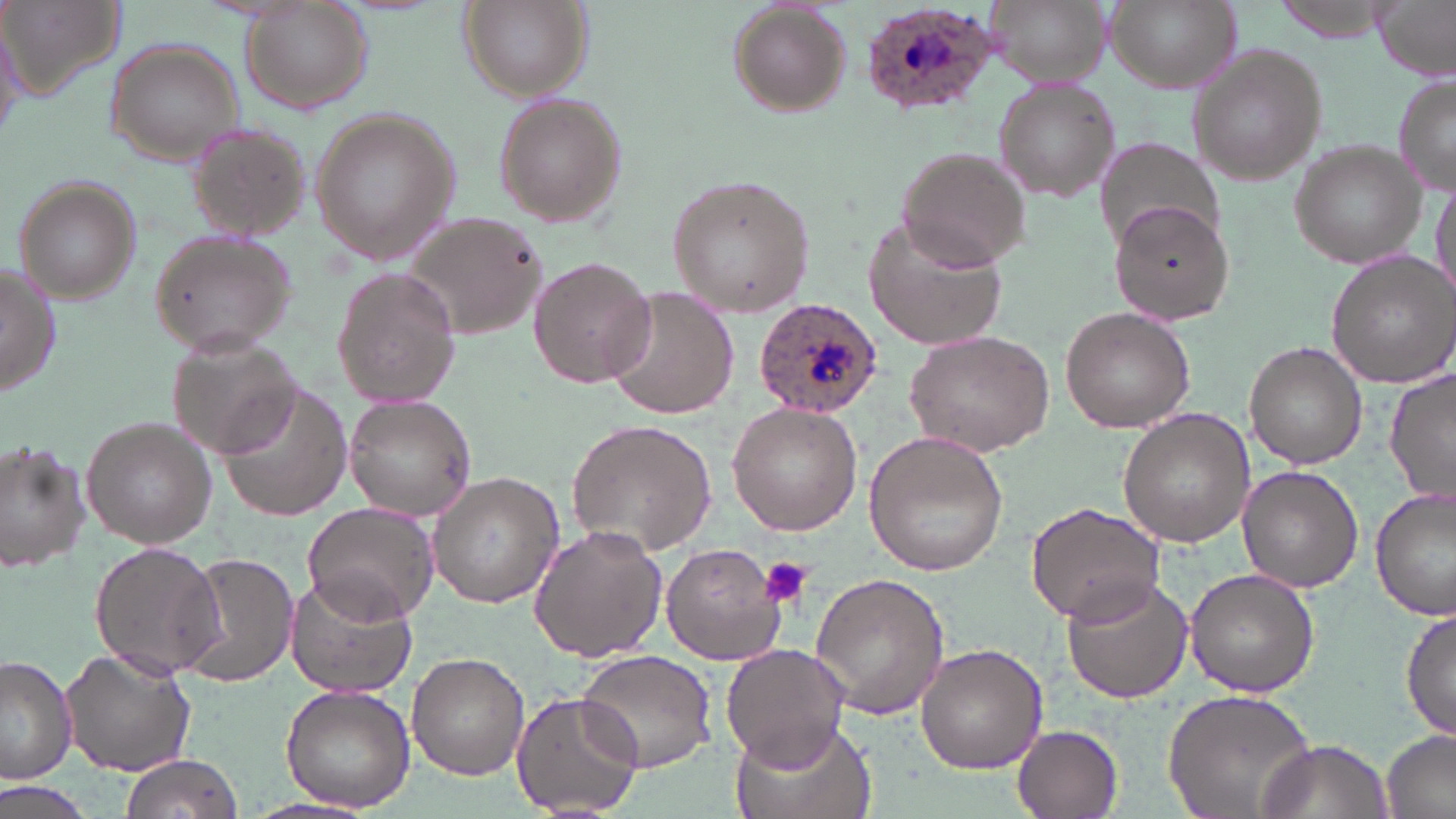

Summary:
  - Coordinate format: approximate bounding boxes as (x1,y1)-(x2,y2) corner pairs in pixels
  - Plasmodium ovale-infected red blood cell locations: (864,4)-(1002,114), (756,298)-(883,415)
  - Uninfected red blood cell locations: (1,0)-(124,102), (453,0)-(592,101), (989,0)-(1110,85), (1104,0)-(1242,95), (1374,0)-(1455,78), (235,1)-(376,116), (1267,1)-(1398,40), (731,2)-(852,113), (103,36)-(244,165), (1187,45)-(1327,186), (1393,71)-(1455,196), (996,80)-(1119,204), (492,94)-(626,229), (312,109)-(459,263), (187,123)-(309,241), (1289,139)-(1428,268), (1094,140)-(1224,256), (895,145)-(1032,271), (667,173)-(816,319), (11,175)-(143,305), (1430,175)-(1455,304), (1108,202)-(1237,326), (398,210)-(549,344), (864,218)-(1011,352), (147,229)-(297,357), (1326,251)-(1456,389), (527,256)-(658,389), (0,265)-(62,399), (332,271)-(463,407), (606,286)-(739,420), (1060,307)-(1195,432), (903,330)-(1056,457), (165,331)-(301,462), (1241,340)-(1368,470), (1384,369)-(1456,508), (215,384)-(351,522), (346,394)-(479,520), (726,403)-(863,535), (1120,410)-(1254,546), (81,418)-(220,547), (567,418)-(718,555), (864,432)-(1009,576), (0,440)-(92,576), (1237,467)-(1363,592), (426,472)-(565,610), (1372,488)-(1455,620), (303,500)-(441,626), (1025,502)-(1166,626), (528,524)-(666,662), (88,539)-(226,681), (662,542)-(782,664), (177,553)-(300,688), (1185,569)-(1319,697), (809,572)-(952,722), (284,573)-(418,700), (1062,574)-(1193,704), (1401,606)-(1456,745), (915,643)-(1047,772), (721,644)-(848,766), (61,646)-(196,775), (576,650)-(715,772), (407,652)-(528,779), (0,655)-(77,783), (280,683)-(417,812), (1161,685)-(1321,819), (511,689)-(644,818), (726,714)-(876,819), (1011,722)-(1124,819), (1382,730)-(1456,819), (1259,737)-(1392,818), (117,753)-(243,819), (0,782)-(90,819)
  - Platelet locations: (757,553)-(815,611)
  - Slide-level diagnosis: Plasmodium ovale
  - Preparation: thin blood smear
  - Magnification: 1000x
  - Modality: optical microscopy
  - Stain: May-Grünwald-Giemsa
  - Image size: 1456×819 pixels
  - Field of view: one of a larger specimen